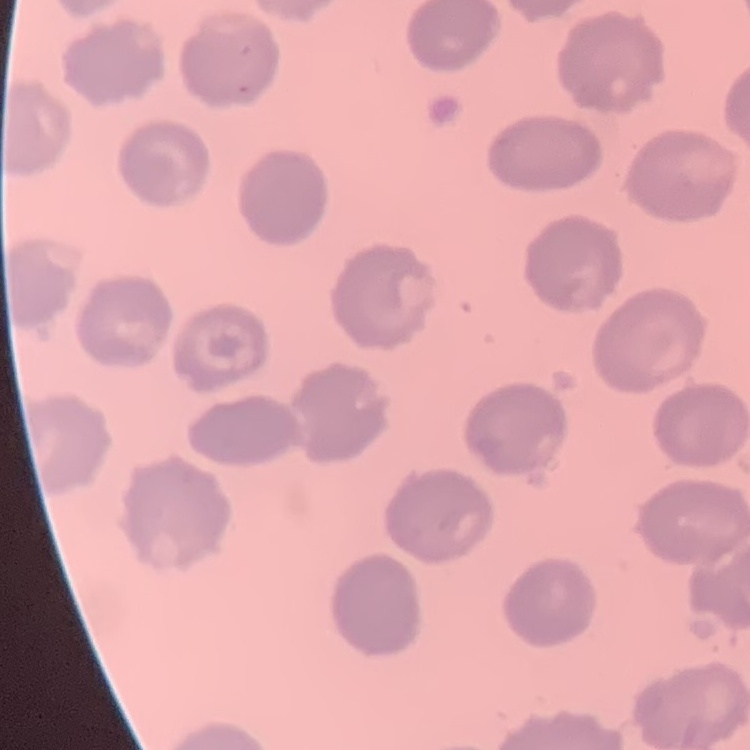
{
  "red_blood_cell_morphology": "no rouleaux formation",
  "image_type": "one tile cut from a larger photomicrograph",
  "stain": "Field's or Giemsa",
  "preparation": "thin blood smear"
}